Give the position of each P. falciparum parasite with its life-cycle stage, each leukocyte, and any debris.
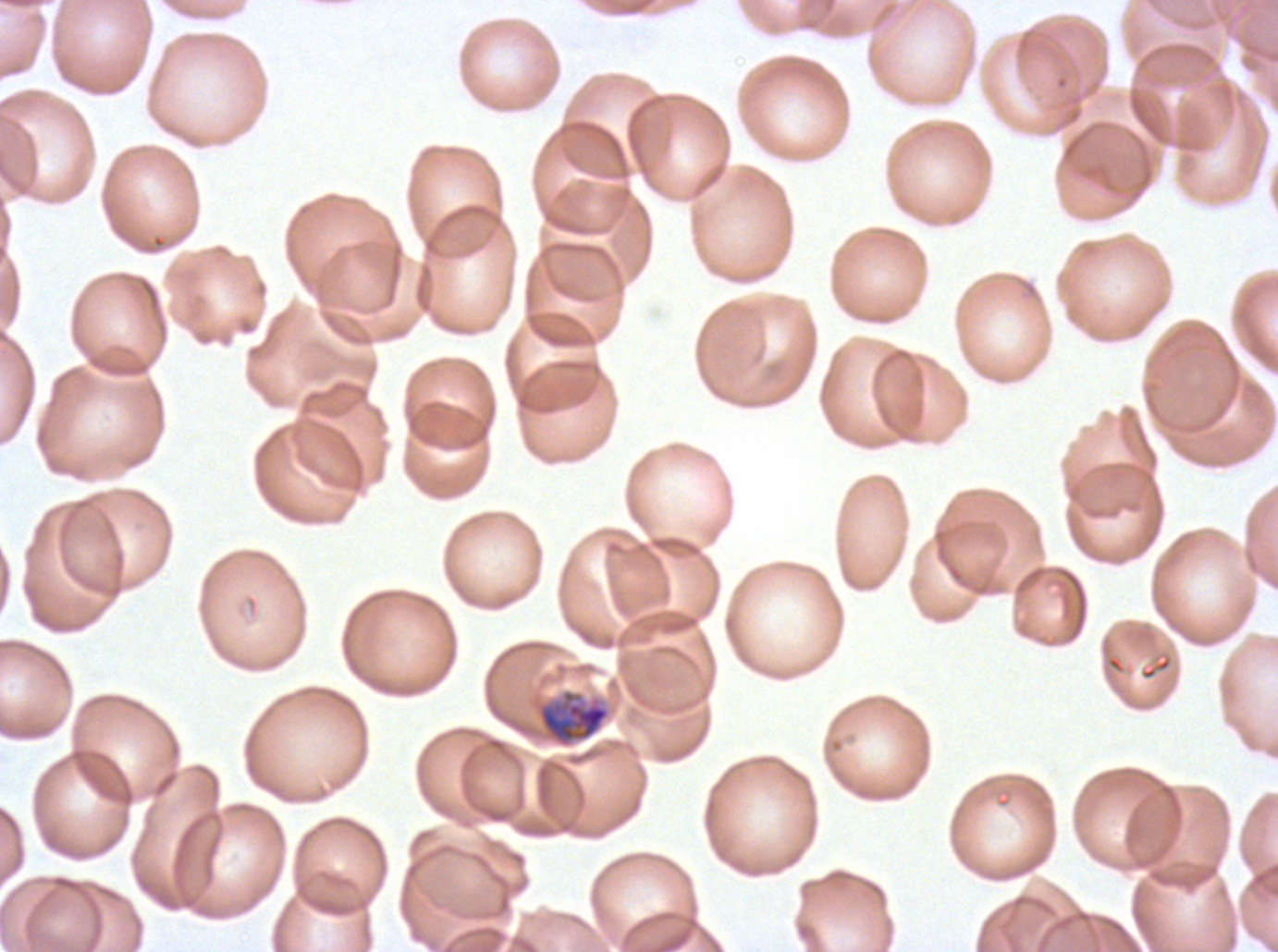
Approximate bounding boxes as {x1, y1, x2, y2} in pixels.
Mid trophozoites: {537, 689, 610, 747}.
No rings, late-ring/early-trophozoite forms, late trophozoites, early schizonts, late schizonts, segmenters, gametocytes, leukocytes, or debris observed.

{
  "field_of_view": "sub-image separated from a larger composite",
  "specimen": "P. falciparum cultured ex vivo for 24 to 48 hours, from a patient in The Gambia",
  "stain": "Giemsa",
  "preparation": "thin blood film",
  "image_size": "1278×952 pixels"
}